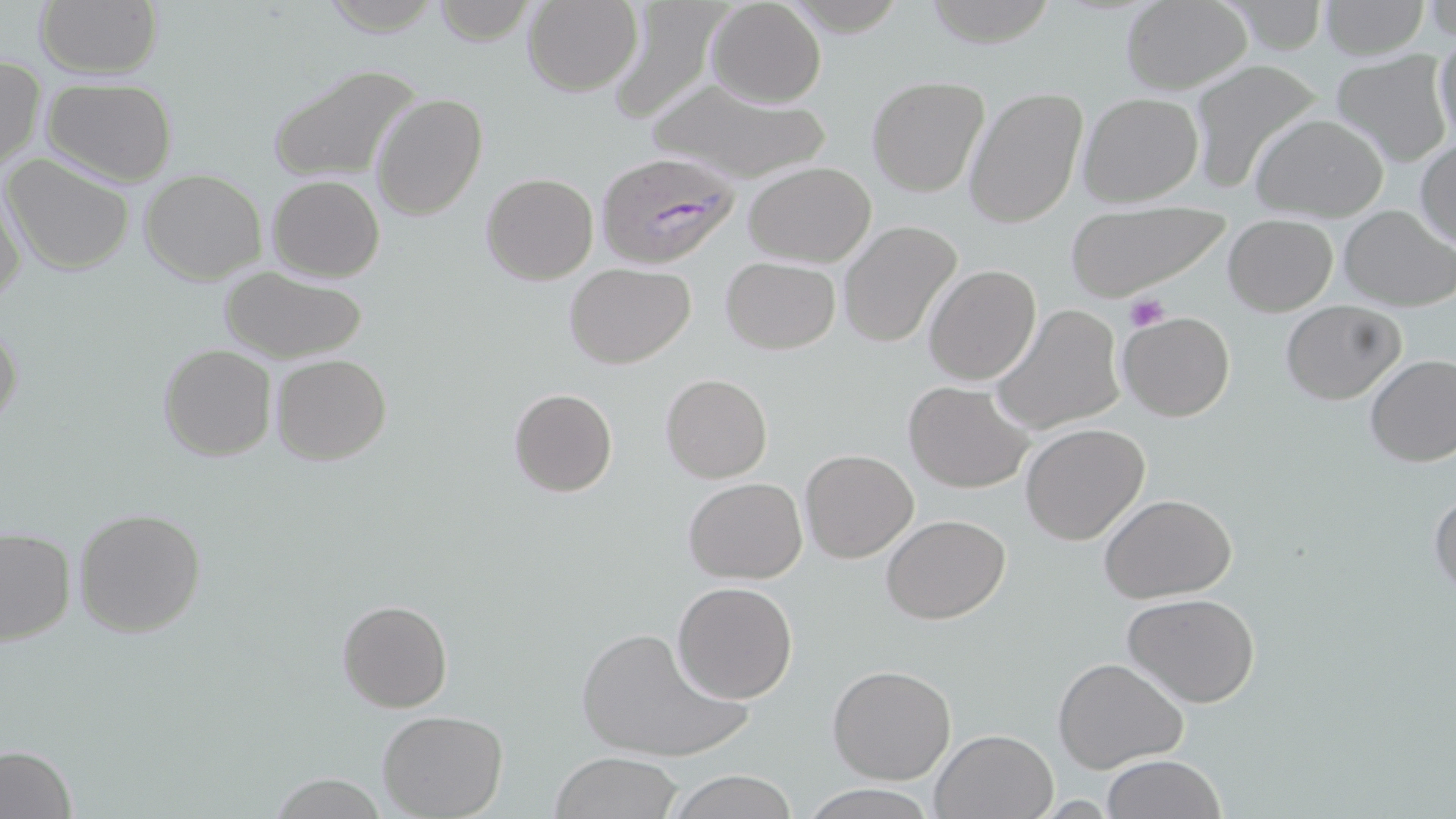

Approximate bounding boxes as [x1, y1, x2, y2] in pixels. Uninfected red blood cell locations: [35, 0, 162, 80], [921, 0, 1059, 47], [522, 1, 642, 96], [602, 1, 723, 126], [705, 1, 827, 108], [1119, 1, 1252, 94], [1316, 1, 1431, 60], [314, 2, 446, 35], [432, 2, 537, 45], [1432, 32, 1456, 148], [1330, 50, 1452, 168], [1, 56, 46, 172], [1190, 61, 1322, 197], [267, 63, 424, 183], [867, 75, 990, 198], [643, 78, 835, 184], [42, 79, 178, 187], [963, 87, 1087, 229], [1076, 91, 1203, 207], [371, 93, 488, 222], [1250, 112, 1390, 223], [1414, 141, 1455, 249], [3, 153, 136, 276], [743, 162, 875, 267], [138, 169, 267, 285], [480, 173, 598, 286], [266, 175, 386, 282], [1, 184, 27, 308], [1064, 200, 1230, 300], [1338, 204, 1454, 311], [1223, 214, 1337, 315], [839, 220, 965, 351], [721, 256, 840, 353], [564, 263, 695, 367], [218, 264, 370, 365], [924, 264, 1041, 386], [1279, 300, 1405, 405], [991, 306, 1126, 434], [1117, 310, 1235, 421], [0, 318, 25, 437], [157, 345, 276, 462], [270, 353, 391, 465], [1365, 355, 1456, 468], [661, 372, 773, 483], [904, 381, 1036, 493], [508, 388, 618, 497], [1020, 423, 1150, 545], [800, 449, 919, 564], [683, 477, 807, 584], [1429, 490, 1456, 601], [1099, 494, 1237, 604], [74, 507, 206, 638], [881, 514, 1010, 624], [0, 527, 75, 647], [671, 581, 798, 702], [1121, 592, 1262, 710], [337, 599, 453, 713], [577, 622, 750, 763], [1053, 655, 1189, 773], [828, 663, 957, 785], [378, 708, 508, 818], [929, 728, 1058, 818], [0, 744, 80, 819], [548, 752, 686, 819], [1102, 754, 1225, 819], [664, 770, 801, 819], [265, 775, 394, 817], [798, 783, 935, 818]. Platelet locations: [1123, 294, 1169, 333]. Plasmodium falciparum-infected red blood cell locations: [593, 153, 740, 270]. Slide-level diagnosis: Plasmodium falciparum. Thin blood smear. Image is 1456×819 pixels. 1000x magnification. Light microscopy. Single field of view. May-Grünwald-Giemsa-stained preparation.